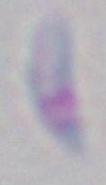 Photomicrograph. Toxoplasma gondii is seen. Captured at 1000x magnification.